Outline each Plasmodium ovale-infected red blood cell.
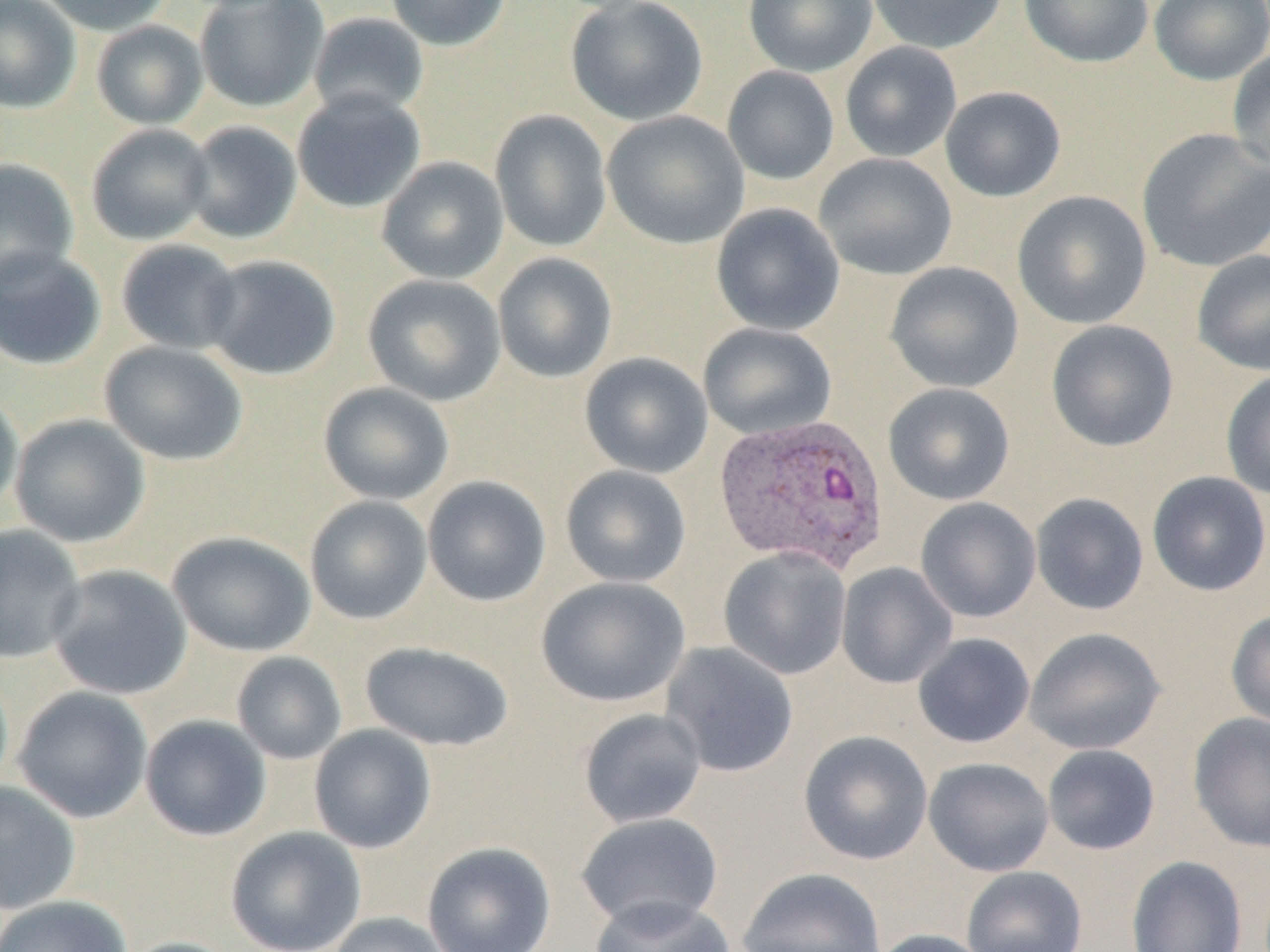

Approximate bounding boxes as [x1, y1, x2, y2] in pixels.
Plasmodium ovale-infected red blood cells: [713, 412, 890, 575].

Summary:
  - Uninfected red blood cell locations: [0, 0, 81, 113], [34, 0, 173, 36], [386, 0, 512, 51], [743, 0, 879, 77], [865, 0, 1008, 54], [1018, 0, 1154, 68], [1149, 0, 1270, 86], [193, 1, 330, 113], [565, 1, 709, 126], [308, 13, 429, 121], [91, 20, 208, 129], [840, 41, 962, 163], [1226, 47, 1270, 175], [722, 66, 840, 185], [940, 86, 1066, 203], [292, 89, 426, 213], [490, 109, 612, 252], [602, 110, 750, 249], [182, 120, 302, 244], [86, 123, 215, 245], [1136, 128, 1270, 273], [813, 152, 957, 281], [376, 156, 509, 284], [0, 159, 79, 288], [1012, 190, 1152, 329], [711, 203, 845, 336], [115, 239, 244, 354], [0, 246, 107, 370], [1191, 249, 1270, 376], [492, 252, 617, 383], [203, 255, 341, 380], [885, 262, 1024, 393], [362, 274, 506, 405], [1046, 320, 1179, 452], [698, 323, 837, 441], [99, 340, 248, 466], [579, 352, 712, 478], [1220, 368, 1270, 501], [318, 382, 455, 506], [883, 382, 1015, 505], [0, 387, 23, 520], [10, 414, 151, 547], [560, 465, 692, 588], [1146, 471, 1270, 597], [422, 475, 551, 607], [1030, 492, 1149, 615], [304, 495, 433, 625], [915, 497, 1041, 623], [0, 525, 87, 664], [168, 530, 316, 657], [718, 546, 852, 680], [836, 562, 957, 689], [48, 564, 193, 700], [536, 576, 690, 707], [1226, 608, 1270, 729], [1024, 627, 1166, 755], [912, 633, 1036, 748], [360, 641, 514, 751], [660, 641, 799, 778], [231, 651, 347, 765], [13, 686, 153, 823], [578, 708, 707, 828], [1188, 712, 1270, 852], [140, 714, 271, 841], [308, 724, 437, 853], [798, 730, 933, 865], [1042, 744, 1160, 855], [923, 757, 1054, 877], [0, 781, 81, 915], [574, 812, 724, 932], [225, 827, 367, 952], [421, 841, 556, 952], [1126, 855, 1247, 952], [961, 865, 1088, 952], [737, 867, 886, 952], [588, 894, 736, 952], [0, 895, 133, 952], [325, 912, 454, 952], [868, 928, 995, 952], [117, 936, 246, 952]
  - Slide-level diagnosis: Plasmodium ovale
  - Field of view: single
  - Modality: optical microscopy
  - Magnification: 1000x
  - Preparation: thin blood film
  - Image size: 1270×952 pixels